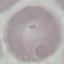

result: negative for malaria parasites
image_type: automatically extracted cell patch, resized to 64 × 64 pixels
capture: smartphone camera at the microscope eyepiece
stain: Giemsa
preparation: thin blood smear